Assess the morphology of the erythrocytes.
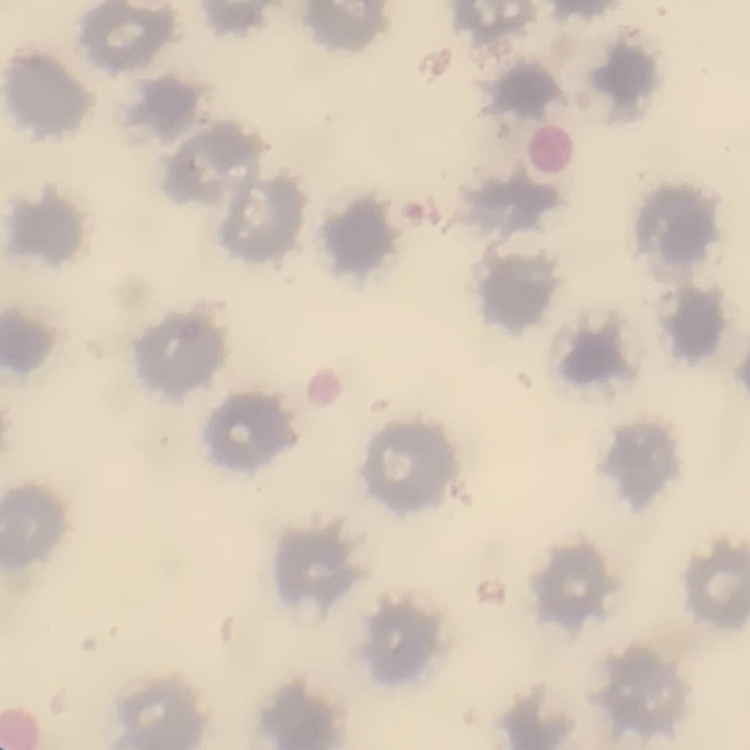

No rouleaux formation.

stain: Field's or Giemsa
image_type: one tile cut from a larger photomicrograph
preparation: thin blood film